Describe the morphology of the red blood cells.
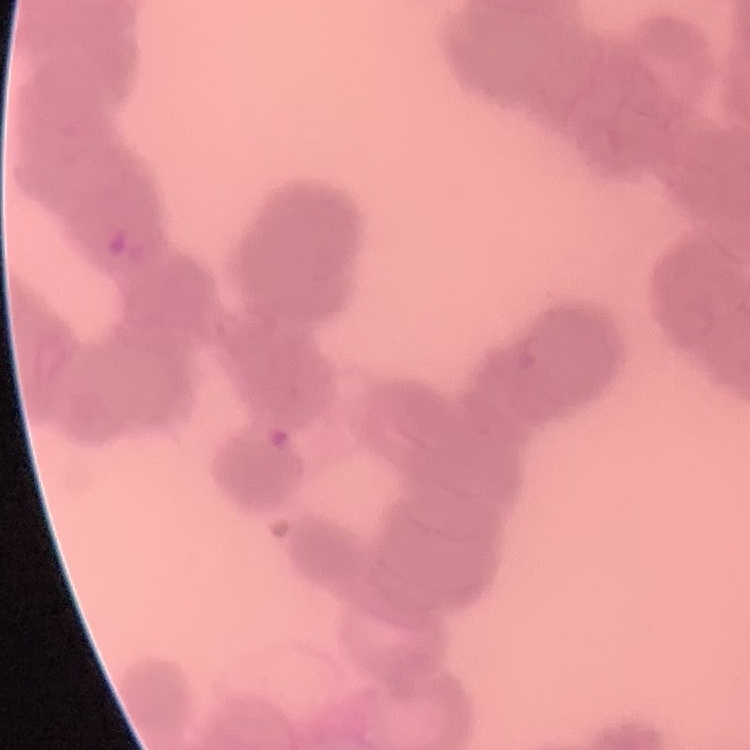
Rouleaux formation.

image type = square crop of a larger photomicrograph
preparation = thin peripheral smear
stain = Field's or Giemsa